Outline each blood parasite and name the species.
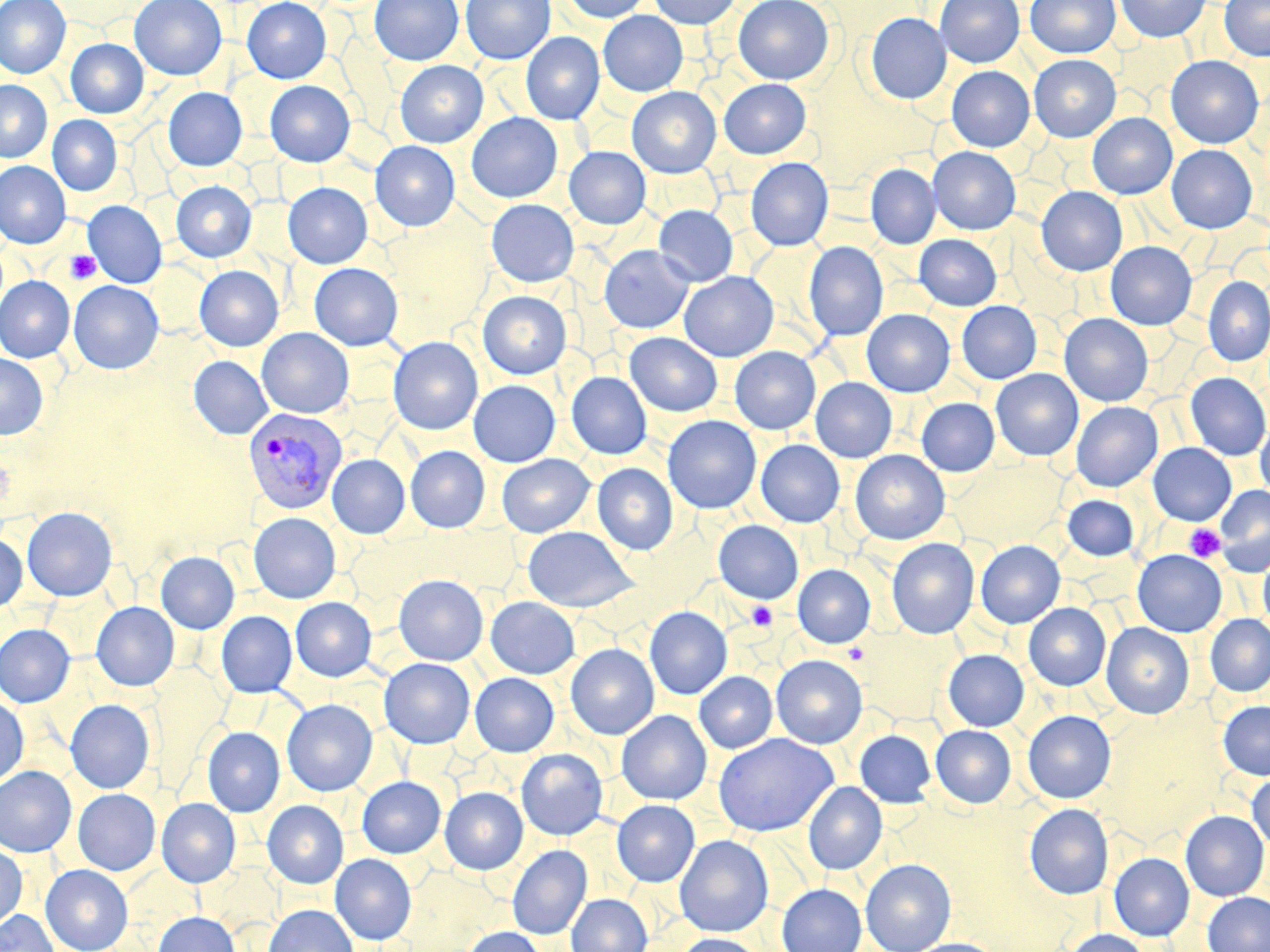

Approximate bounding boxes as [x1, y1, x2, y2] in pixels.
Plasmodium vivax-infected red blood cells: [242, 407, 347, 514].
No Plasmodium falciparum, Plasmodium ovale, Plasmodium malariae, Babesia divergens, or Trypanosoma brucei observed.

Summary:
  - Uninfected red blood cell locations: [0, 0, 71, 79], [130, 0, 227, 80], [242, 0, 332, 83], [257, 0, 344, 166], [370, 0, 463, 65], [461, 0, 555, 64], [562, 0, 652, 23], [649, 0, 741, 29], [734, 0, 834, 85], [935, 0, 1025, 67], [1025, 0, 1120, 58], [1115, 0, 1210, 42], [1220, 0, 1270, 61], [599, 11, 688, 96], [865, 13, 951, 104], [520, 32, 604, 124], [66, 38, 148, 118], [1028, 54, 1121, 142], [1166, 56, 1264, 148], [395, 60, 488, 148], [947, 66, 1034, 152], [719, 79, 811, 158], [0, 80, 52, 162], [265, 80, 355, 167], [627, 87, 721, 178], [163, 88, 247, 171], [1087, 112, 1177, 199], [466, 113, 563, 203], [47, 115, 122, 196], [370, 140, 460, 231], [1166, 145, 1257, 233], [564, 147, 651, 229], [928, 147, 1021, 235], [745, 157, 833, 250], [0, 161, 71, 248], [866, 164, 941, 249], [171, 180, 257, 262], [282, 182, 372, 268], [1036, 187, 1127, 276], [486, 199, 579, 287], [83, 200, 167, 288], [654, 205, 738, 286], [914, 234, 1001, 310], [1106, 241, 1196, 330], [804, 242, 888, 341], [598, 245, 694, 334], [309, 262, 403, 351], [195, 265, 284, 351], [679, 271, 778, 361], [0, 276, 74, 362], [1203, 276, 1270, 366], [68, 280, 164, 374], [478, 291, 571, 379], [957, 301, 1042, 384], [862, 309, 955, 397], [1060, 314, 1153, 406], [257, 328, 354, 418], [625, 332, 722, 416], [388, 337, 483, 435], [730, 346, 821, 435], [0, 353, 48, 439], [189, 356, 273, 439], [991, 369, 1083, 461], [566, 371, 652, 460], [1185, 372, 1270, 461], [811, 378, 897, 462], [468, 380, 560, 467], [916, 398, 1000, 476], [1071, 401, 1162, 492], [663, 416, 761, 513], [1255, 421, 1270, 502], [756, 440, 844, 527], [1148, 443, 1236, 525], [406, 446, 490, 532], [850, 450, 950, 545], [496, 454, 594, 537], [328, 455, 410, 538], [592, 463, 678, 555], [1214, 485, 1270, 576], [1062, 495, 1139, 561], [22, 507, 117, 601], [249, 512, 341, 604], [714, 520, 804, 604], [523, 525, 638, 612], [0, 534, 27, 612], [887, 538, 979, 639], [975, 540, 1065, 628], [1132, 549, 1227, 637], [156, 552, 240, 633], [1258, 552, 1270, 635], [793, 565, 875, 648], [393, 575, 488, 666], [291, 597, 376, 681], [486, 597, 580, 679], [91, 602, 179, 691], [1024, 603, 1111, 691], [645, 607, 732, 699], [216, 611, 297, 697], [1205, 614, 1270, 696], [1101, 623, 1194, 719], [0, 624, 75, 707], [565, 644, 659, 739], [943, 649, 1029, 731], [771, 655, 867, 749], [379, 658, 475, 748], [694, 671, 777, 753], [470, 673, 558, 756], [0, 696, 29, 788], [65, 699, 155, 793], [282, 699, 377, 796], [1218, 700, 1270, 779], [616, 710, 712, 804], [1023, 710, 1116, 803], [931, 725, 1016, 807], [202, 727, 285, 817], [855, 730, 936, 808], [714, 733, 837, 836], [516, 748, 608, 840], [0, 766, 76, 856], [1247, 773, 1270, 852], [357, 776, 446, 858], [804, 782, 887, 874], [440, 787, 528, 874], [73, 788, 160, 875], [156, 798, 241, 887], [263, 800, 348, 888], [612, 800, 700, 886], [1025, 803, 1114, 899], [1180, 810, 1269, 901], [675, 835, 774, 937], [0, 842, 27, 931], [507, 845, 592, 939], [1109, 853, 1194, 940], [330, 854, 416, 944], [861, 859, 956, 952], [41, 865, 133, 952], [776, 884, 867, 952], [1202, 892, 1270, 952], [566, 893, 652, 952], [263, 904, 358, 952], [0, 911, 59, 952], [153, 912, 240, 952], [462, 927, 547, 952], [1064, 929, 1153, 952], [673, 933, 765, 952], [907, 938, 1001, 952]
  - Platelet locations: [65, 250, 101, 284], [1185, 524, 1225, 562], [747, 602, 777, 630]
  - Slide-level diagnosis: Plasmodium vivax
  - Field of view: one of a larger specimen
  - Magnification: 1000x
  - Image size: 1270×952 pixels
  - Preparation: thin blood film
  - Modality: optical microscopy
  - Stain: May-Grünwald-Giemsa